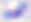
identification = Toxoplasma gondii
modality = micrograph
magnification = 400x